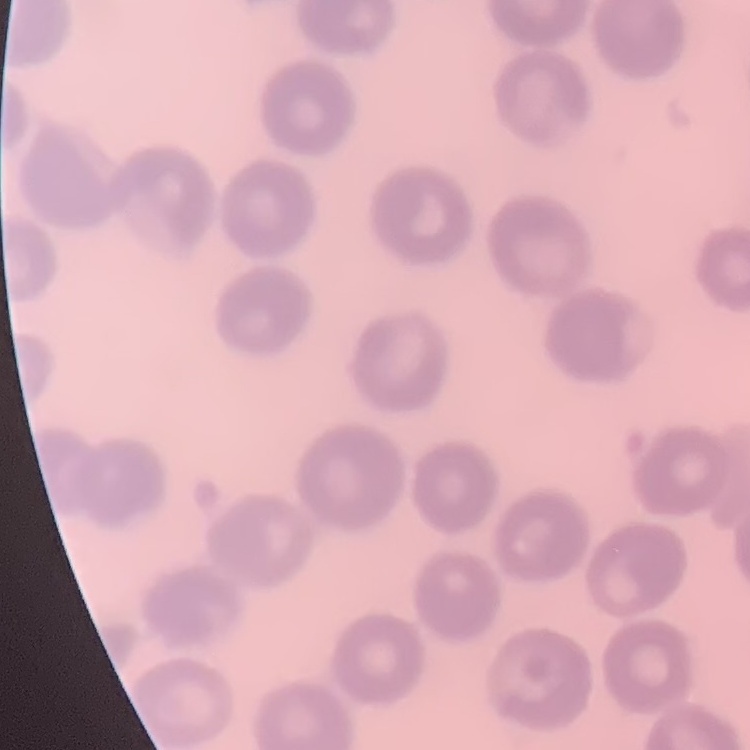

Summary:
  - Red blood cell morphology: no rouleaux formation
  - Image type: one tile cut from a larger photomicrograph
  - Preparation: thin peripheral smear
  - Stain: Field's or Giemsa